Locate every Plasmodium parasite.
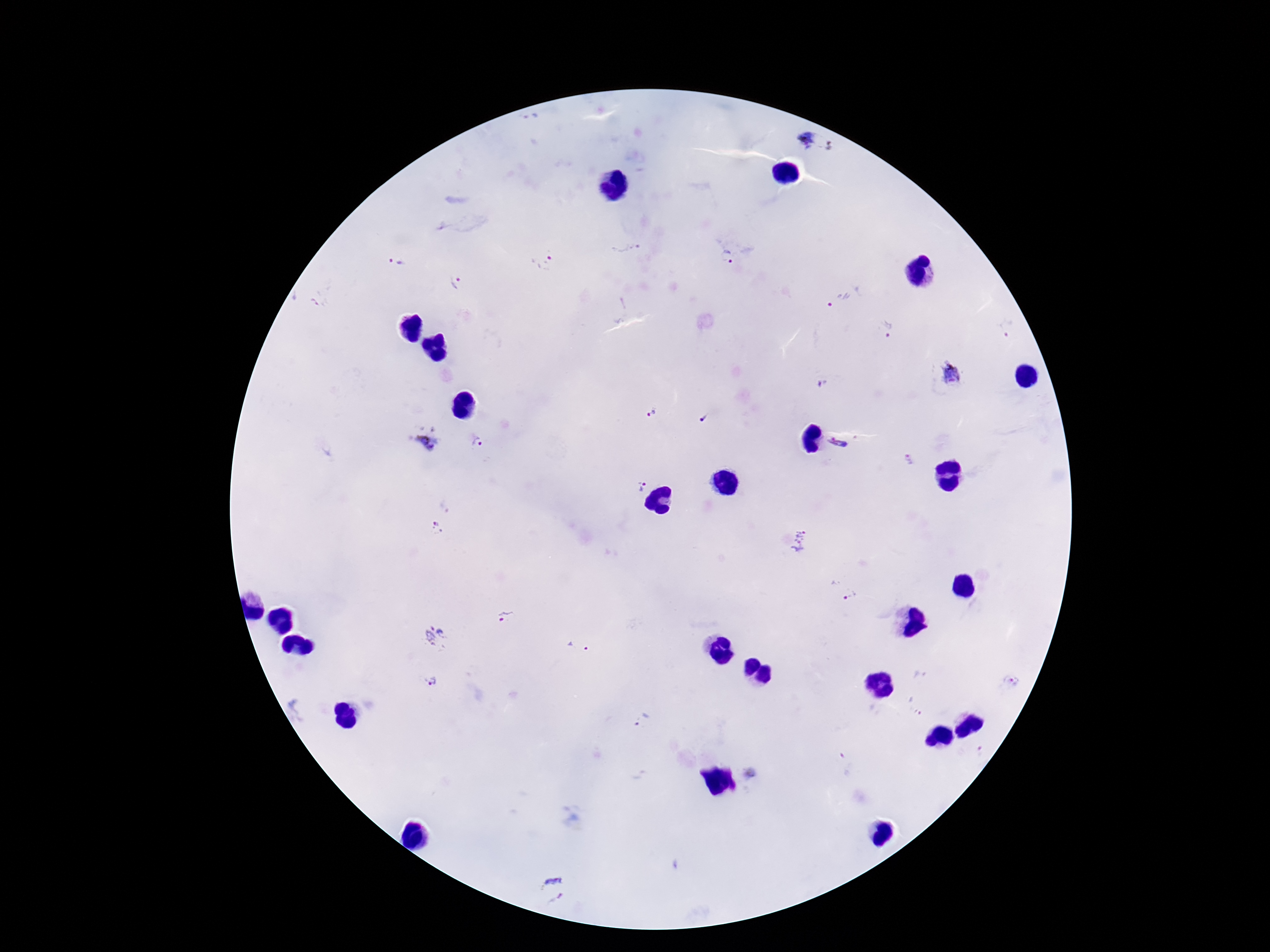

Approximate centers as [x, y] in pixels.
Plasmodium parasites: [807, 140], [832, 145], [627, 248], [726, 256], [397, 262], [544, 262], [455, 283], [844, 294], [888, 326], [1007, 328], [951, 375], [822, 384], [651, 414], [706, 418], [425, 438], [476, 443], [839, 444], [910, 460], [640, 489], [436, 529], [803, 541], [842, 588], [505, 617], [437, 638], [577, 647], [431, 681], [1015, 683], [306, 705], [916, 705], [645, 722], [981, 750], [845, 762], [752, 774], [553, 891].

image size = 1270×952 pixels
capture = smartphone camera through the microscope eyepiece
preparation = thick blood smear
field of view = single
patient malaria status = infected
magnification = 100x
stain = Giemsa